Report the malaria status of this cell.
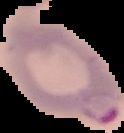
It is parasitized.

Summary:
  - Image size: 124×133 pixels
  - Preparation: thin blood film
  - Image type: segmented cell region on a black background